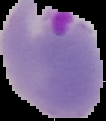
image size = 106×121 pixels
image type = segmented cell region on a black background
preparation = thin blood smear
malaria status = parasitized